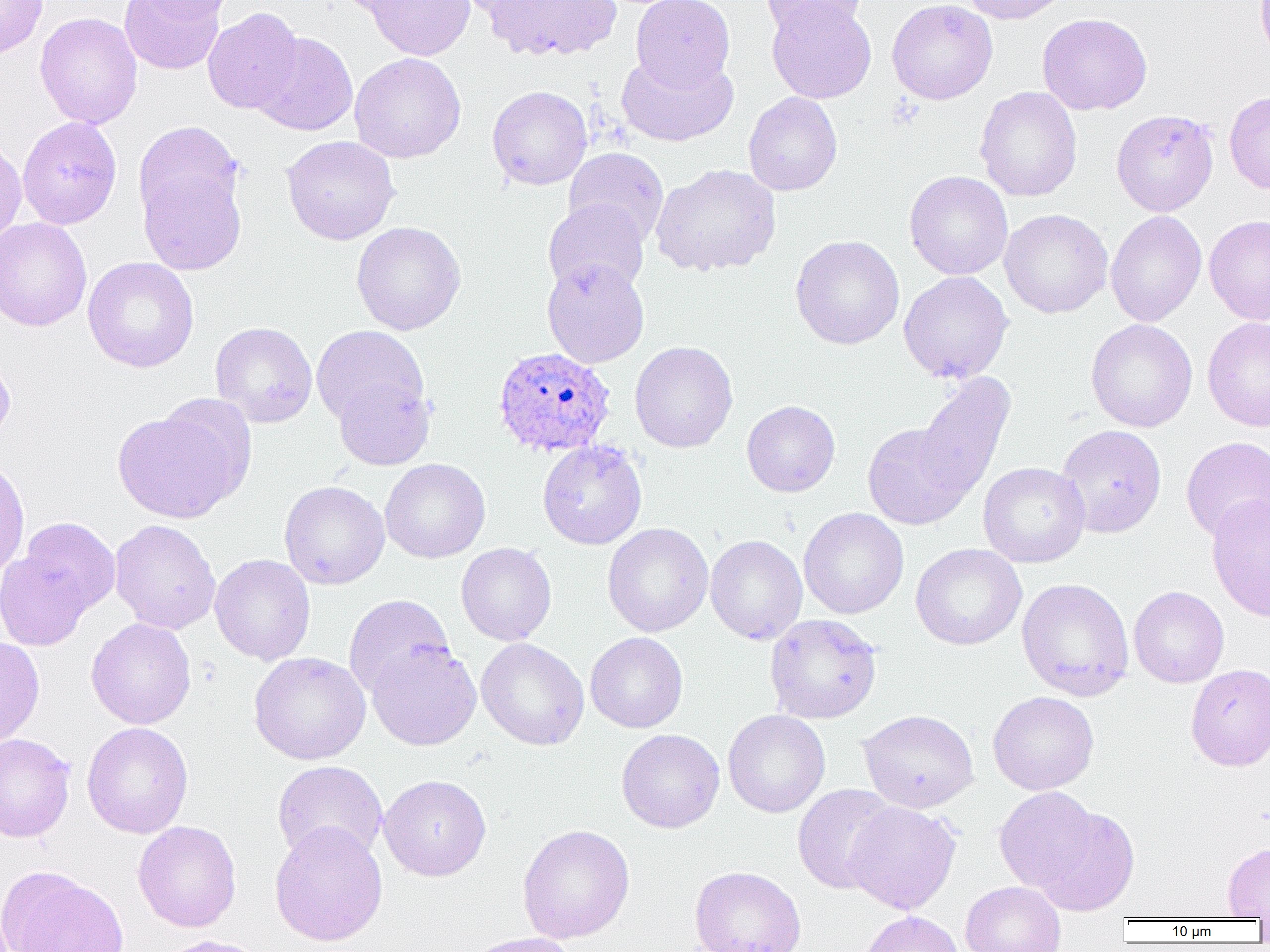

{
  "slide_level_diagnosis": "Plasmodium ovale",
  "image_size": "1270×952 pixels",
  "uninfected_red_blood_cell_locations": "approximate bounding boxes as (x1, y1, x2, y2) in pixels: (0, 0, 48, 59), (119, 0, 225, 75), (136, 0, 237, 22), (331, 0, 422, 17), (363, 0, 476, 61), (451, 0, 550, 18), (483, 0, 622, 61), (631, 0, 735, 91), (761, 0, 868, 40), (887, 0, 998, 105), (958, 0, 1071, 25), (767, 1, 877, 103), (202, 7, 303, 114), (35, 12, 142, 129), (1037, 13, 1153, 115), (252, 32, 358, 136), (615, 50, 739, 147), (350, 52, 466, 163), (487, 85, 592, 190), (974, 86, 1082, 202), (1224, 91, 1270, 195), (743, 92, 843, 196), (1111, 109, 1219, 216), (17, 116, 123, 229), (133, 121, 244, 229), (281, 135, 400, 245), (0, 139, 27, 248), (563, 147, 669, 246), (138, 163, 247, 275), (650, 164, 781, 277), (904, 170, 1013, 280), (543, 199, 649, 297), (999, 208, 1113, 318), (1105, 210, 1207, 327), (1204, 214, 1270, 325), (0, 217, 92, 332), (351, 221, 466, 335), (790, 235, 905, 350), (83, 257, 199, 372), (542, 258, 650, 368), (898, 271, 1013, 384), (1202, 317, 1270, 432), (1086, 318, 1197, 432), (210, 321, 317, 428), (311, 325, 429, 430), (629, 341, 738, 453), (0, 349, 15, 448), (913, 371, 1016, 503), (333, 377, 435, 470), (741, 400, 840, 497), (112, 401, 250, 524), (862, 422, 974, 530), (1055, 424, 1167, 538), (1181, 436, 1270, 543), (537, 440, 647, 549), (0, 457, 30, 581), (380, 458, 490, 563), (978, 461, 1090, 568), (279, 480, 390, 590), (1207, 493, 1270, 622), (798, 507, 909, 619), (15, 517, 121, 620), (110, 519, 221, 634), (603, 523, 713, 637), (705, 534, 807, 645), (456, 542, 557, 646), (911, 543, 1027, 650), (0, 549, 94, 651), (210, 554, 315, 665), (1017, 577, 1135, 701), (1128, 586, 1229, 688), (343, 594, 454, 699), (765, 614, 882, 724), (86, 617, 196, 729), (585, 632, 688, 733), (0, 636, 45, 747), (476, 637, 589, 750), (366, 641, 482, 751), (249, 651, 370, 764), (1185, 663, 1270, 770), (988, 691, 1099, 794), (723, 709, 830, 818), (858, 709, 979, 813), (82, 722, 193, 838), (616, 729, 724, 833), (0, 733, 76, 843), (272, 760, 388, 864), (378, 774, 492, 881), (793, 784, 899, 894), (994, 786, 1100, 894), (844, 801, 962, 914), (1032, 805, 1140, 916), (133, 821, 241, 932), (269, 821, 389, 946), (517, 824, 635, 943), (1222, 842, 1270, 920), (0, 864, 130, 952), (689, 865, 806, 952), (960, 881, 1066, 952), (858, 910, 964, 952), (462, 932, 582, 952), (158, 934, 271, 952)",
  "modality": "optical microscopy",
  "magnification": "1000x",
  "preparation": "thin blood smear",
  "field_of_view": "single",
  "plasmodium_ovale_infected_red_blood_cell_locations": "approximate bounding boxes as (x1, y1, x2, y2) in pixels: (492, 346, 616, 457)"
}